Comment on the morphology of the red blood cells.
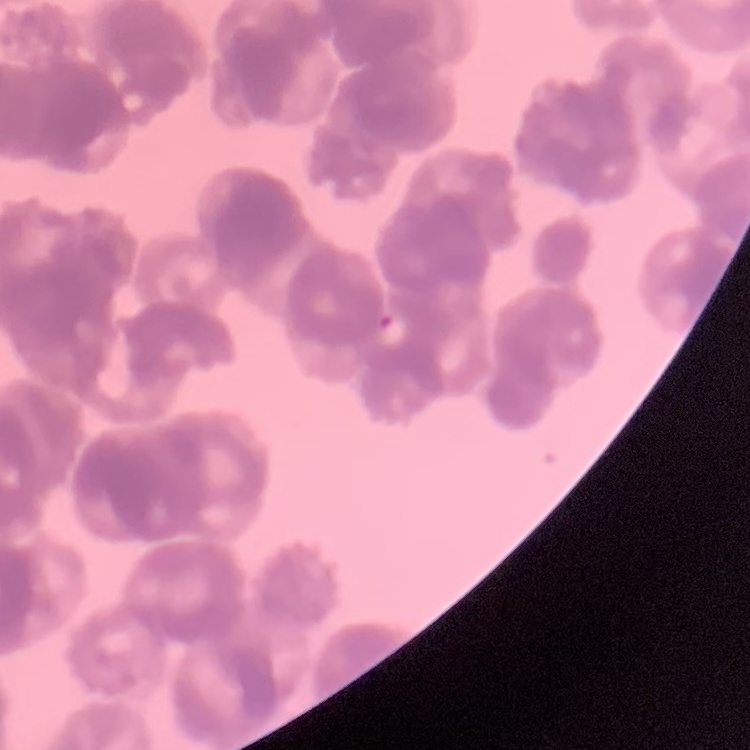

Rouleaux formation.

image type = square crop of a larger photomicrograph
stain = Field's or Giemsa
preparation = thin peripheral smear